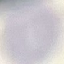
Malaria status: uninfected. Thin smear of blood. Acquired by smartphone through the microscope eyepiece. Giemsa-stained preparation. Automatically extracted cell patch, resized to 64 × 64 pixels.